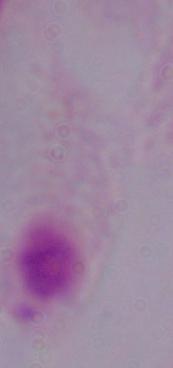
A trichomonad is shown. 1000x magnification. Micrograph.